Report the malaria status of this cell.
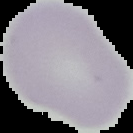
Uninfected.

image_size: 133×133 pixels
image_type: segmented cell region with the area outside set to black
preparation: thin blood smear